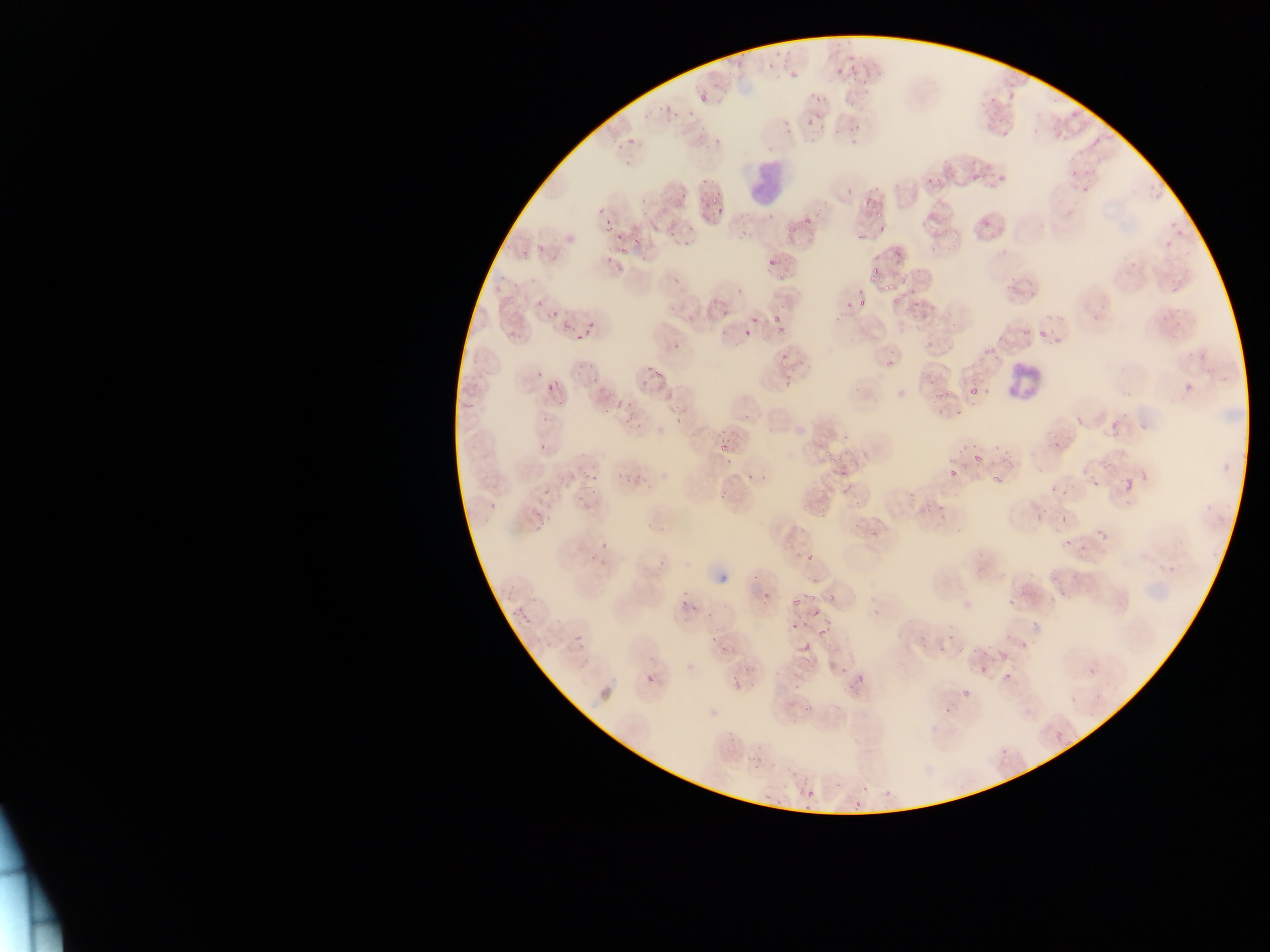
Approximate bounding boxes as [left, top, right, bottom] in pixels. Leukocyte locations: [750, 152, 796, 197], [1002, 364, 1041, 399]. Malaria parasite locations: [843, 44, 861, 60], [730, 53, 750, 70], [769, 54, 779, 74], [788, 65, 801, 80], [848, 65, 866, 80], [832, 67, 842, 77], [1004, 86, 1020, 101], [810, 91, 825, 104], [693, 93, 705, 108], [974, 94, 998, 111], [659, 103, 673, 118], [674, 105, 692, 123], [834, 112, 849, 134], [805, 118, 813, 127], [1049, 120, 1066, 144], [849, 121, 864, 145], [1000, 122, 1015, 140], [627, 137, 634, 145], [1094, 138, 1102, 147], [1067, 159, 1079, 179], [926, 171, 941, 186], [987, 173, 1006, 195], [971, 174, 980, 181], [699, 177, 707, 185], [1077, 179, 1094, 203], [843, 189, 854, 199], [860, 191, 875, 210], [639, 195, 651, 203], [708, 195, 721, 208], [597, 203, 607, 212], [712, 206, 727, 218], [765, 213, 775, 223], [979, 213, 997, 233], [800, 218, 812, 229], [880, 220, 887, 247], [601, 221, 612, 232], [939, 224, 954, 238], [854, 225, 869, 239], [628, 232, 639, 249], [666, 233, 674, 239], [611, 236, 623, 242], [888, 244, 900, 257], [616, 247, 626, 259], [763, 256, 776, 274], [867, 267, 882, 282], [881, 276, 899, 294], [902, 278, 917, 296], [855, 294, 870, 309], [887, 295, 900, 308], [842, 299, 851, 310], [906, 300, 930, 322], [714, 306, 731, 319], [546, 308, 559, 322], [773, 311, 787, 323], [749, 314, 763, 334], [774, 320, 787, 333], [557, 321, 568, 335], [575, 323, 592, 341], [506, 325, 518, 338], [1037, 325, 1051, 341], [743, 328, 753, 337], [1049, 335, 1062, 346], [923, 338, 936, 351], [673, 342, 679, 350], [781, 351, 794, 366], [884, 354, 901, 369], [648, 363, 662, 381], [538, 368, 550, 378], [588, 368, 601, 381], [780, 374, 793, 385], [634, 377, 649, 391], [544, 384, 555, 397], [968, 388, 977, 397], [931, 389, 941, 402], [665, 394, 672, 409], [616, 396, 623, 409], [460, 398, 478, 409], [602, 402, 617, 413], [954, 408, 963, 420], [672, 414, 680, 422], [537, 436, 551, 452], [719, 437, 731, 455], [822, 438, 839, 465], [971, 449, 985, 462], [721, 456, 734, 469], [747, 463, 759, 481], [633, 465, 643, 480], [583, 468, 601, 481], [989, 468, 999, 486], [615, 470, 623, 483], [836, 471, 853, 493], [944, 471, 957, 479], [1091, 480, 1100, 489], [1124, 480, 1134, 491], [539, 484, 554, 497], [904, 484, 914, 501], [1050, 484, 1057, 492], [816, 499, 834, 517], [935, 504, 947, 511], [529, 515, 546, 533], [1060, 516, 1067, 525], [866, 522, 879, 539], [657, 524, 663, 532], [1098, 526, 1108, 534], [1060, 538, 1067, 549], [588, 543, 602, 565], [1077, 544, 1086, 555], [1099, 545, 1109, 561], [1059, 585, 1067, 601], [759, 591, 771, 602], [677, 592, 692, 609], [791, 592, 805, 610], [1003, 593, 1019, 608], [689, 606, 699, 625], [516, 607, 527, 618], [809, 608, 819, 623], [946, 620, 964, 642], [783, 623, 794, 631], [819, 623, 829, 638], [914, 625, 926, 645], [574, 633, 584, 643], [718, 639, 729, 652], [937, 639, 947, 652], [1024, 641, 1031, 651], [800, 642, 812, 652], [998, 646, 1008, 660], [835, 660, 848, 678], [999, 664, 1020, 689], [969, 665, 987, 676], [1088, 666, 1096, 675], [640, 671, 656, 689], [727, 674, 744, 693], [790, 675, 801, 691], [853, 676, 869, 691], [960, 688, 967, 701], [802, 702, 814, 712], [941, 702, 955, 720], [1056, 733, 1063, 742], [750, 735, 761, 764], [994, 745, 1011, 758], [877, 782, 892, 795], [807, 788, 816, 797], [765, 793, 778, 806], [854, 800, 861, 808] | approximate [x, y] pixel centers of objects too small to bound: [682, 196], [810, 556]. One field of view. Image is 1270×952 pixels. Sample from Ghana. Photographed through a microscope with a mobile-phone camera. Thin blood film.